Give the extent of all Plasmodium falciparum-infected red blood cells.
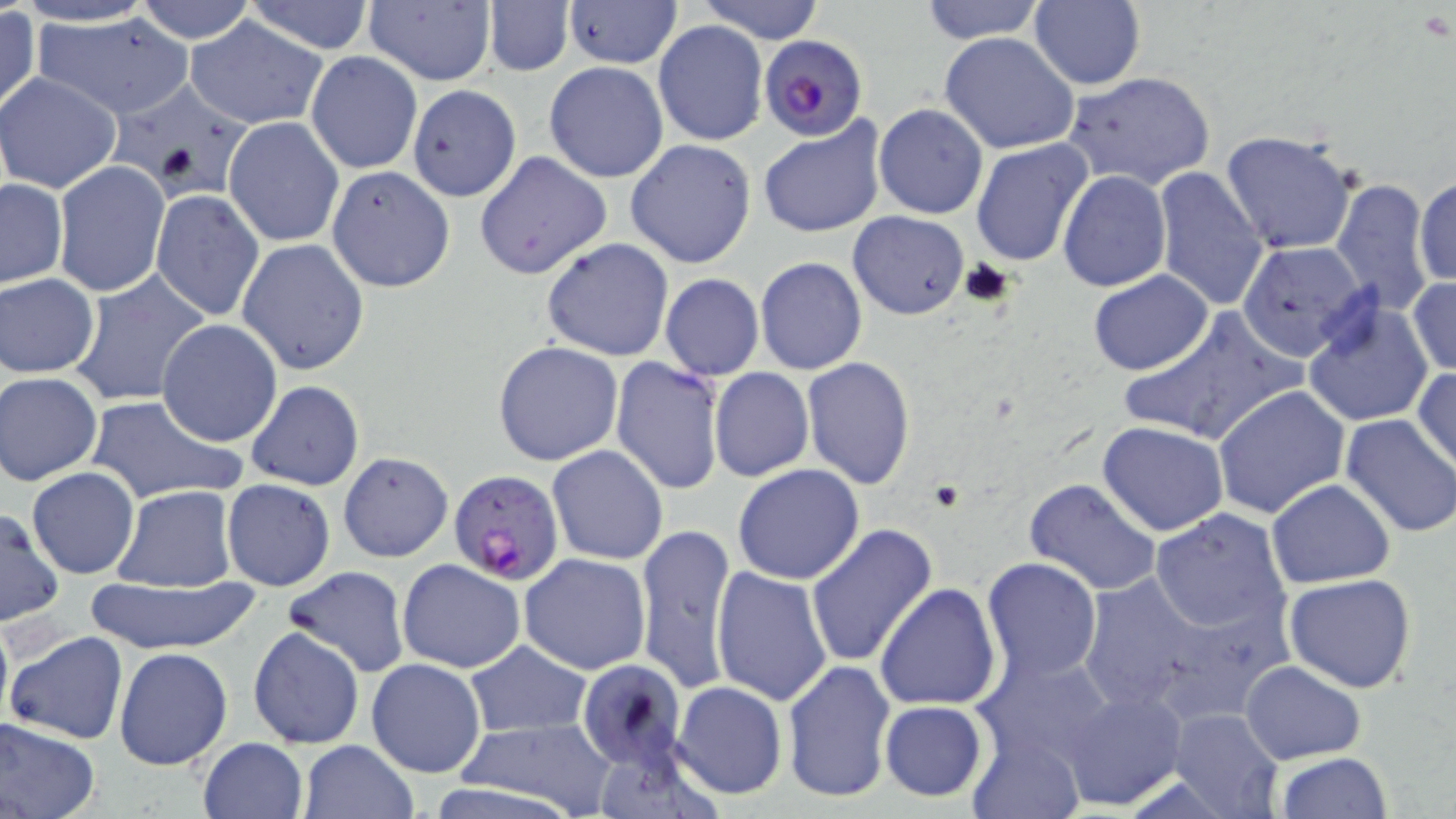
Approximate bounding boxes as named x1/y1/x2/y2 corners in pixels.
Plasmodium falciparum-infected red blood cells: (x1=760, y1=35, x2=866, y2=140), (x1=447, y1=470, x2=564, y2=586).

Uninfected red blood cell locations: (x1=10, y1=0, x2=164, y2=28), (x1=134, y1=0, x2=257, y2=45), (x1=243, y1=0, x2=377, y2=54), (x1=363, y1=0, x2=495, y2=86), (x1=697, y1=0, x2=825, y2=43), (x1=918, y1=0, x2=1047, y2=42), (x1=1028, y1=0, x2=1145, y2=91), (x1=563, y1=1, x2=683, y2=69), (x1=483, y1=3, x2=572, y2=76), (x1=1, y1=7, x2=41, y2=118), (x1=31, y1=10, x2=195, y2=121), (x1=186, y1=16, x2=328, y2=128), (x1=653, y1=20, x2=768, y2=146), (x1=939, y1=32, x2=1082, y2=154), (x1=305, y1=51, x2=423, y2=175), (x1=544, y1=61, x2=670, y2=183), (x1=1064, y1=69, x2=1216, y2=190), (x1=0, y1=72, x2=123, y2=193), (x1=114, y1=80, x2=257, y2=202), (x1=407, y1=84, x2=523, y2=202), (x1=874, y1=104, x2=988, y2=219), (x1=224, y1=117, x2=345, y2=247), (x1=759, y1=117, x2=887, y2=238), (x1=1220, y1=130, x2=1358, y2=254), (x1=625, y1=138, x2=756, y2=269), (x1=970, y1=138, x2=1094, y2=268), (x1=475, y1=152, x2=611, y2=281), (x1=52, y1=162, x2=169, y2=296), (x1=327, y1=165, x2=456, y2=294), (x1=1151, y1=166, x2=1270, y2=310), (x1=1058, y1=170, x2=1171, y2=292), (x1=1415, y1=173, x2=1454, y2=290), (x1=1330, y1=176, x2=1435, y2=317), (x1=0, y1=179, x2=68, y2=289), (x1=149, y1=190, x2=265, y2=323), (x1=848, y1=212, x2=967, y2=320), (x1=236, y1=238, x2=370, y2=376), (x1=541, y1=238, x2=674, y2=361), (x1=1238, y1=241, x2=1371, y2=362), (x1=756, y1=257, x2=866, y2=374), (x1=1088, y1=269, x2=1214, y2=377), (x1=67, y1=270, x2=213, y2=409), (x1=660, y1=273, x2=764, y2=381), (x1=1, y1=274, x2=100, y2=378), (x1=1408, y1=276, x2=1456, y2=376), (x1=1301, y1=298, x2=1435, y2=427), (x1=1119, y1=306, x2=1302, y2=446), (x1=156, y1=319, x2=284, y2=447), (x1=493, y1=339, x2=623, y2=465), (x1=610, y1=357, x2=725, y2=495), (x1=802, y1=357, x2=917, y2=488), (x1=1413, y1=366, x2=1455, y2=473), (x1=709, y1=367, x2=814, y2=482), (x1=1, y1=372, x2=103, y2=486), (x1=245, y1=380, x2=363, y2=492), (x1=1212, y1=385, x2=1350, y2=519), (x1=84, y1=394, x2=246, y2=507), (x1=1339, y1=414, x2=1456, y2=538), (x1=1097, y1=421, x2=1229, y2=537), (x1=547, y1=445, x2=669, y2=566), (x1=337, y1=451, x2=454, y2=562), (x1=733, y1=463, x2=866, y2=584), (x1=27, y1=466, x2=140, y2=578), (x1=1023, y1=477, x2=1161, y2=597), (x1=1265, y1=478, x2=1395, y2=587), (x1=221, y1=479, x2=335, y2=591), (x1=114, y1=486, x2=237, y2=592), (x1=0, y1=508, x2=64, y2=626), (x1=1149, y1=508, x2=1290, y2=636), (x1=634, y1=522, x2=735, y2=695), (x1=804, y1=525, x2=938, y2=670), (x1=520, y1=553, x2=652, y2=675), (x1=982, y1=557, x2=1102, y2=683), (x1=396, y1=558, x2=525, y2=673), (x1=282, y1=566, x2=409, y2=678), (x1=710, y1=567, x2=833, y2=706), (x1=1070, y1=567, x2=1253, y2=716), (x1=1285, y1=572, x2=1419, y2=693), (x1=86, y1=574, x2=259, y2=654), (x1=875, y1=583, x2=1002, y2=711), (x1=0, y1=611, x2=13, y2=734), (x1=247, y1=625, x2=365, y2=749), (x1=5, y1=630, x2=129, y2=746), (x1=465, y1=640, x2=593, y2=736), (x1=113, y1=647, x2=233, y2=771), (x1=973, y1=652, x2=1118, y2=769), (x1=366, y1=658, x2=487, y2=776), (x1=782, y1=658, x2=897, y2=804), (x1=576, y1=660, x2=688, y2=769), (x1=1240, y1=660, x2=1365, y2=764), (x1=671, y1=680, x2=788, y2=800), (x1=1057, y1=688, x2=1185, y2=811), (x1=879, y1=700, x2=987, y2=801), (x1=1168, y1=708, x2=1284, y2=818), (x1=0, y1=717, x2=101, y2=819), (x1=453, y1=719, x2=616, y2=812), (x1=968, y1=733, x2=1082, y2=819), (x1=197, y1=736, x2=307, y2=819), (x1=298, y1=739, x2=418, y2=819), (x1=1274, y1=751, x2=1392, y2=818). Slide-level diagnosis: Plasmodium falciparum. Captured at 1000x magnification. Thin blood film. May-Grünwald-Giemsa stain. Image is 1456×819 pixels. Single field of view. Light microscopy.